Classify this cell by malaria status.
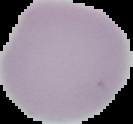
Uninfected.

{
  "preparation": "thin blood smear",
  "image_type": "segmented cell region with the area outside set to black",
  "image_size": "133×124 pixels"
}